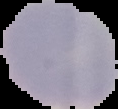
result = negative for malaria parasites
image type = cell region segmented out of the field of view; surrounding area masked to black
preparation = thin blood smear
image size = 118×109 pixels